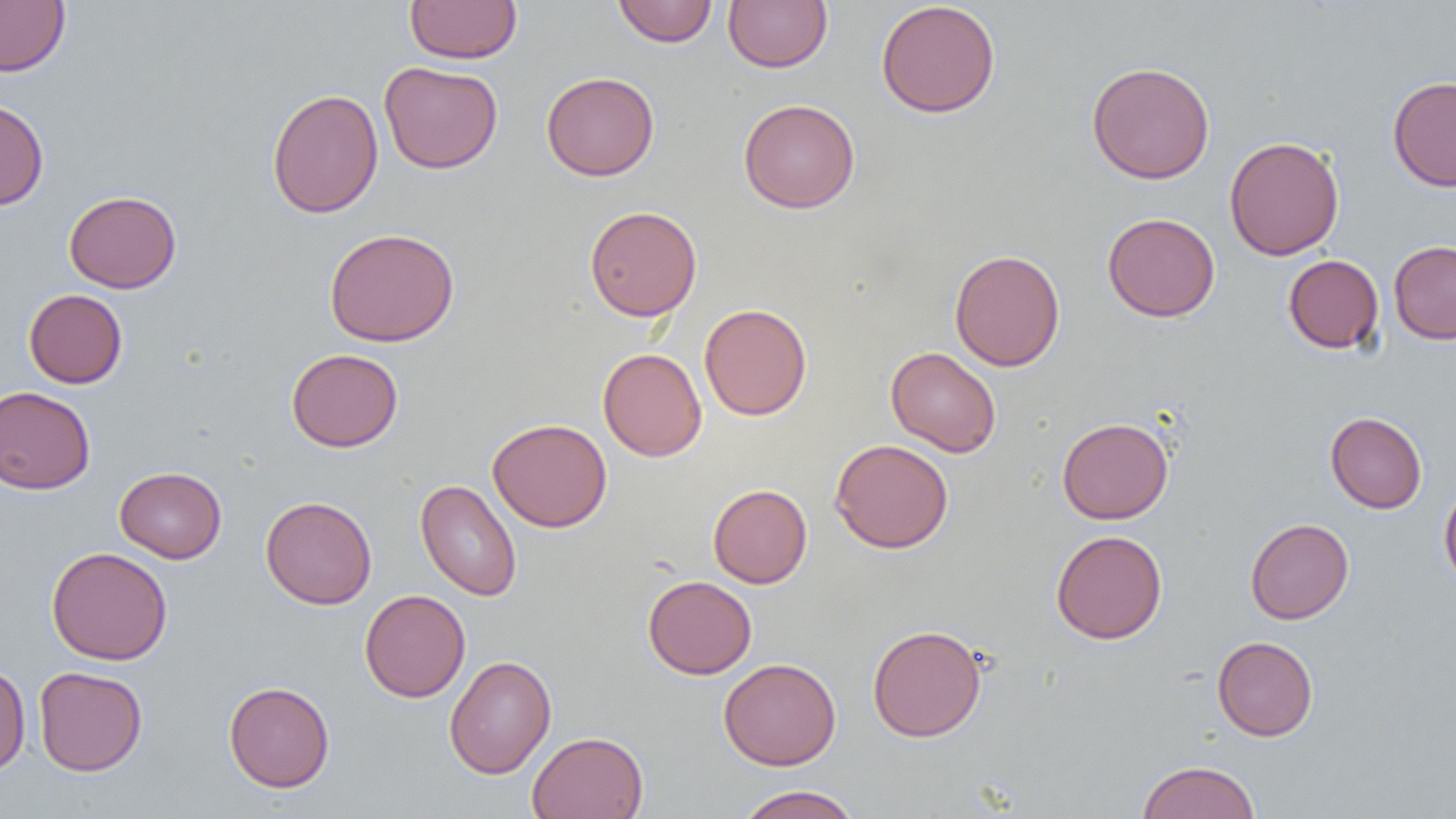
slide-level diagnosis = no evidence of blood parasites
preparation = thin blood smear
uninfected red blood cell locations = approximate bounding boxes as named x1/y1/x2/y2 corners in pixels: (x1=0, y1=0, x2=70, y2=77), (x1=405, y1=0, x2=522, y2=64), (x1=724, y1=0, x2=832, y2=72), (x1=612, y1=1, x2=719, y2=47), (x1=875, y1=1, x2=1001, y2=118), (x1=378, y1=61, x2=503, y2=174), (x1=1086, y1=61, x2=1215, y2=184), (x1=541, y1=71, x2=659, y2=181), (x1=1387, y1=76, x2=1456, y2=191), (x1=266, y1=88, x2=384, y2=219), (x1=0, y1=97, x2=49, y2=210), (x1=739, y1=98, x2=860, y2=213), (x1=1224, y1=135, x2=1344, y2=261), (x1=64, y1=190, x2=182, y2=293), (x1=584, y1=205, x2=702, y2=321), (x1=1102, y1=212, x2=1220, y2=322), (x1=324, y1=227, x2=459, y2=347), (x1=1389, y1=240, x2=1456, y2=344), (x1=950, y1=249, x2=1065, y2=372), (x1=1283, y1=254, x2=1384, y2=354), (x1=24, y1=289, x2=127, y2=388), (x1=699, y1=303, x2=812, y2=420), (x1=886, y1=347, x2=1001, y2=457), (x1=286, y1=348, x2=403, y2=452), (x1=598, y1=348, x2=707, y2=462), (x1=0, y1=385, x2=95, y2=494), (x1=1325, y1=411, x2=1427, y2=514), (x1=1057, y1=417, x2=1174, y2=524), (x1=488, y1=418, x2=612, y2=532), (x1=829, y1=439, x2=954, y2=554), (x1=115, y1=466, x2=227, y2=563), (x1=415, y1=479, x2=522, y2=601), (x1=1439, y1=481, x2=1456, y2=590), (x1=708, y1=484, x2=812, y2=588), (x1=260, y1=496, x2=377, y2=609), (x1=1245, y1=518, x2=1354, y2=624), (x1=1050, y1=529, x2=1168, y2=645), (x1=46, y1=546, x2=172, y2=665), (x1=643, y1=575, x2=756, y2=679), (x1=359, y1=589, x2=471, y2=702), (x1=868, y1=623, x2=986, y2=742), (x1=1212, y1=636, x2=1318, y2=741), (x1=444, y1=655, x2=556, y2=779), (x1=718, y1=657, x2=841, y2=770), (x1=0, y1=663, x2=31, y2=775), (x1=33, y1=666, x2=148, y2=776), (x1=223, y1=681, x2=335, y2=792), (x1=527, y1=731, x2=649, y2=819), (x1=1136, y1=760, x2=1260, y2=819), (x1=734, y1=785, x2=862, y2=819)
field of view = single
image size = 1456×819 pixels
magnification = 1000x
modality = light microscopy